Describe the morphology of the red blood cells.
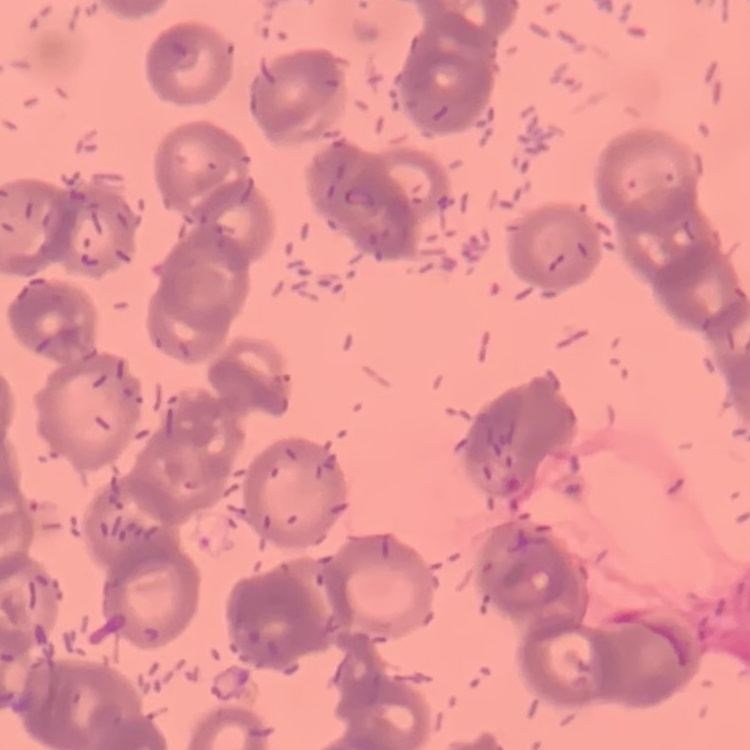

They show rouleaux formation.

{
  "preparation": "thin blood smear",
  "stain": "Field's or Giemsa",
  "image_type": "square crop of a larger photomicrograph"
}